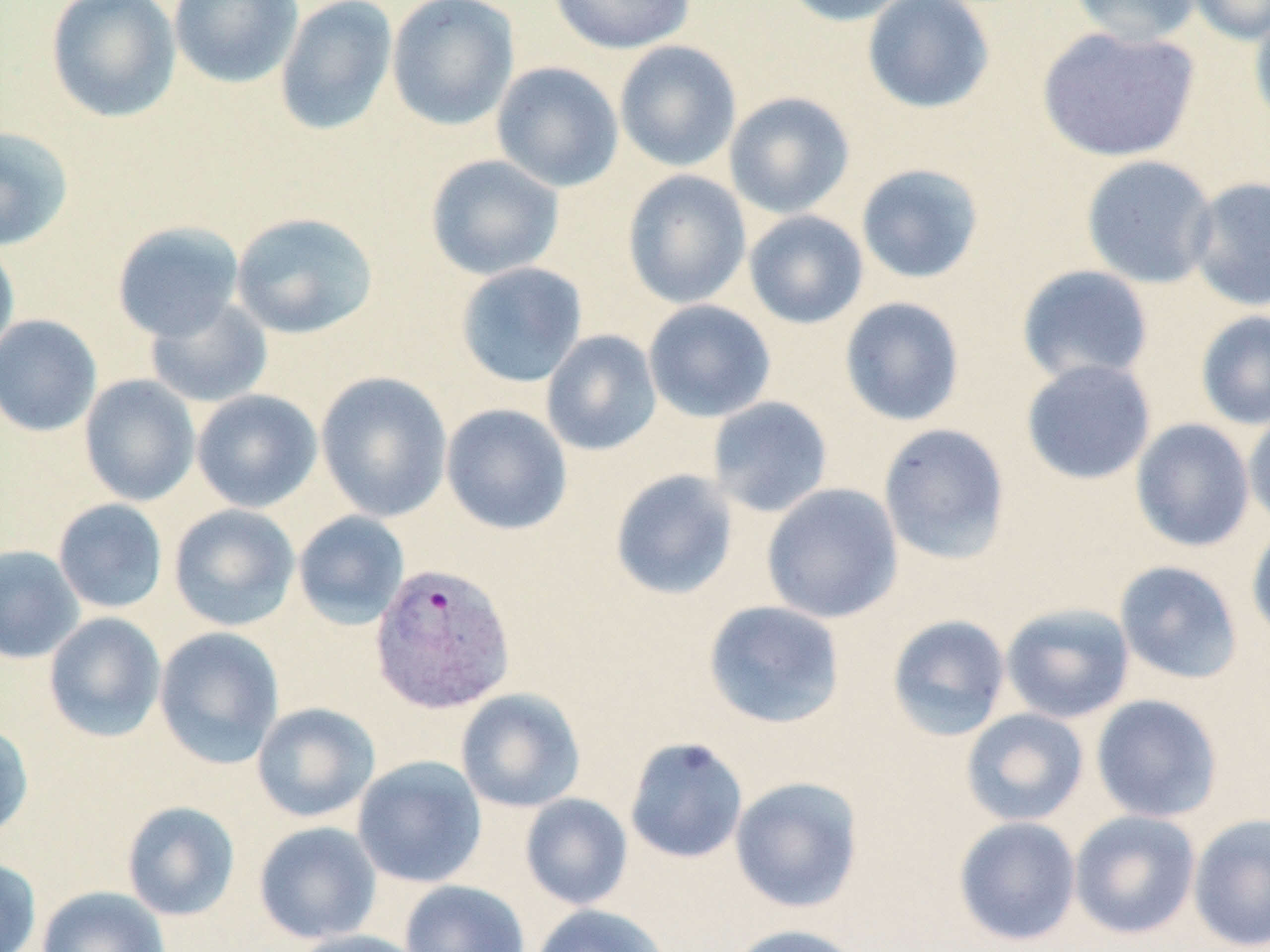
slide-level diagnosis = Plasmodium vivax
stain = May-Grünwald-Giemsa
image size = 1270×952 pixels
magnification = 1000x
field of view = one of a larger specimen
uninfected red blood cell locations = approximate bounding boxes as named x1/y1/x2/y2 corners in pixels: (x1=45, y1=0, x2=182, y2=123), (x1=169, y1=0, x2=303, y2=89), (x1=275, y1=0, x2=398, y2=137), (x1=386, y1=0, x2=520, y2=131), (x1=547, y1=0, x2=696, y2=54), (x1=779, y1=0, x2=914, y2=26), (x1=861, y1=0, x2=995, y2=114), (x1=1069, y1=0, x2=1202, y2=47), (x1=1184, y1=0, x2=1270, y2=45), (x1=1249, y1=7, x2=1270, y2=127), (x1=1036, y1=25, x2=1200, y2=163), (x1=614, y1=41, x2=742, y2=173), (x1=491, y1=61, x2=624, y2=192), (x1=724, y1=92, x2=855, y2=219), (x1=0, y1=125, x2=74, y2=251), (x1=425, y1=154, x2=565, y2=281), (x1=1080, y1=155, x2=1219, y2=289), (x1=855, y1=163, x2=985, y2=284), (x1=622, y1=169, x2=752, y2=309), (x1=1186, y1=176, x2=1270, y2=311), (x1=743, y1=210, x2=868, y2=330), (x1=230, y1=211, x2=379, y2=340), (x1=112, y1=221, x2=245, y2=342), (x1=0, y1=241, x2=20, y2=363), (x1=455, y1=262, x2=588, y2=388), (x1=1016, y1=264, x2=1154, y2=385), (x1=144, y1=296, x2=274, y2=409), (x1=838, y1=296, x2=965, y2=427), (x1=643, y1=300, x2=776, y2=423), (x1=1195, y1=309, x2=1270, y2=430), (x1=0, y1=314, x2=102, y2=437), (x1=541, y1=329, x2=662, y2=456), (x1=1020, y1=358, x2=1157, y2=485), (x1=315, y1=371, x2=453, y2=523), (x1=79, y1=374, x2=201, y2=506), (x1=191, y1=389, x2=323, y2=513), (x1=707, y1=396, x2=833, y2=518), (x1=440, y1=403, x2=573, y2=535), (x1=1243, y1=408, x2=1270, y2=532), (x1=1130, y1=418, x2=1255, y2=553), (x1=878, y1=423, x2=1011, y2=565), (x1=609, y1=469, x2=739, y2=601), (x1=761, y1=483, x2=903, y2=623), (x1=52, y1=498, x2=168, y2=614), (x1=168, y1=503, x2=300, y2=631), (x1=293, y1=511, x2=410, y2=629), (x1=1246, y1=521, x2=1270, y2=645), (x1=0, y1=544, x2=85, y2=665), (x1=1114, y1=560, x2=1243, y2=685), (x1=702, y1=600, x2=846, y2=730), (x1=1000, y1=602, x2=1135, y2=724), (x1=43, y1=612, x2=166, y2=742), (x1=886, y1=614, x2=1011, y2=741), (x1=153, y1=626, x2=285, y2=769), (x1=455, y1=688, x2=585, y2=813), (x1=1090, y1=694, x2=1223, y2=823), (x1=252, y1=701, x2=380, y2=823), (x1=961, y1=708, x2=1089, y2=827), (x1=0, y1=721, x2=34, y2=840), (x1=624, y1=737, x2=748, y2=864), (x1=352, y1=755, x2=487, y2=888), (x1=730, y1=776, x2=864, y2=913), (x1=520, y1=793, x2=633, y2=910), (x1=121, y1=800, x2=241, y2=921), (x1=1069, y1=809, x2=1201, y2=939), (x1=1187, y1=813, x2=1270, y2=951), (x1=953, y1=816, x2=1082, y2=947), (x1=253, y1=821, x2=382, y2=944), (x1=0, y1=857, x2=42, y2=952), (x1=399, y1=880, x2=530, y2=952), (x1=36, y1=886, x2=170, y2=952), (x1=531, y1=903, x2=670, y2=952), (x1=724, y1=924, x2=864, y2=952), (x1=287, y1=929, x2=429, y2=952)
modality = light microscopy
preparation = thin blood film
Plasmodium vivax-infected red blood cell locations = approximate bounding boxes as named x1/y1/x2/y2 corners in pixels: (x1=369, y1=561, x2=517, y2=715)